State which parasite is depicted.
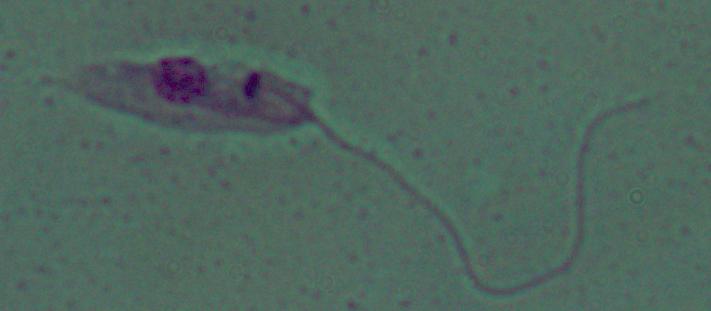
This is Leishmania.

{
  "magnification": "1000x",
  "modality": "photomicrograph"
}